Name the cell type shown.
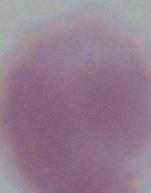
An erythrocyte.

1000x magnification. Micrograph.